Classify this cell by malaria status.
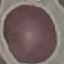
It is uninfected.

Cell patch, automatically extracted from a larger field of view and resized to 64 × 64 pixels. Giemsa-stained preparation. Photographed with a smartphone camera at the microscope eyepiece. Thin smear of blood.